Identify the parasite.
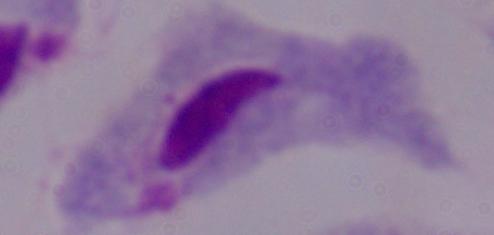
This is a trichomonad.

magnification = 1000x
modality = photomicrograph